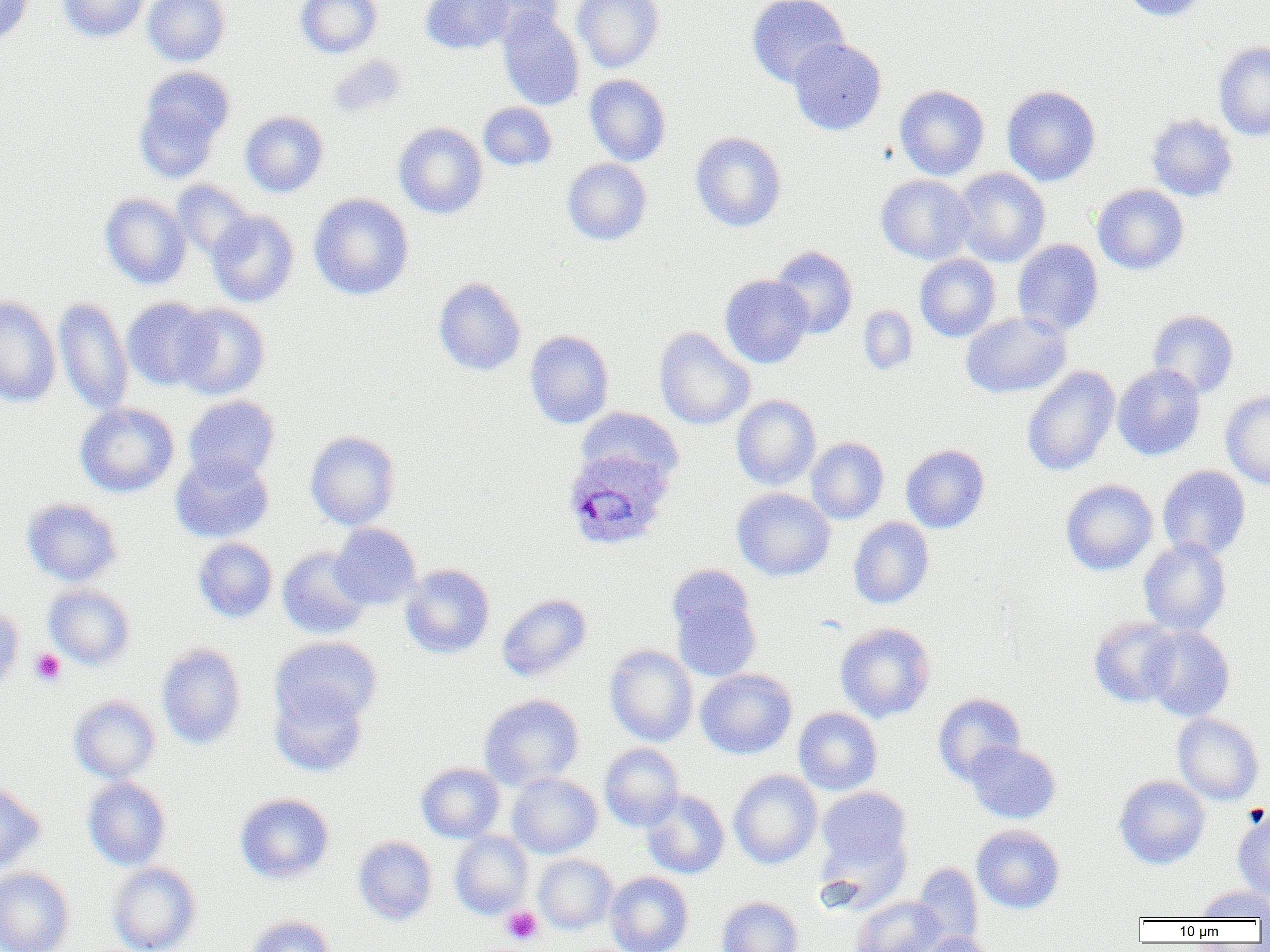

slide-level diagnosis = Plasmodium ovale
platelet locations = approximate bounding boxes as named x1/y1/x2/y2 corners in pixels: (x1=30, y1=648, x2=66, y2=686), (x1=502, y1=906, x2=543, y2=945)
magnification = 1000x
uninfected red blood cell locations = approximate bounding boxes as named x1/y1/x2/y2 corners in pixels: (x1=0, y1=0, x2=34, y2=48), (x1=57, y1=0, x2=151, y2=42), (x1=143, y1=0, x2=230, y2=66), (x1=295, y1=0, x2=382, y2=57), (x1=420, y1=0, x2=513, y2=54), (x1=470, y1=0, x2=563, y2=43), (x1=572, y1=0, x2=664, y2=73), (x1=747, y1=0, x2=849, y2=88), (x1=1118, y1=0, x2=1208, y2=21), (x1=497, y1=9, x2=584, y2=111), (x1=789, y1=38, x2=886, y2=135), (x1=1214, y1=41, x2=1270, y2=140), (x1=327, y1=53, x2=406, y2=118), (x1=134, y1=67, x2=234, y2=179), (x1=584, y1=74, x2=671, y2=166), (x1=894, y1=85, x2=990, y2=180), (x1=1002, y1=85, x2=1101, y2=186), (x1=478, y1=102, x2=556, y2=170), (x1=240, y1=111, x2=328, y2=197), (x1=1146, y1=113, x2=1238, y2=202), (x1=393, y1=122, x2=487, y2=219), (x1=690, y1=131, x2=787, y2=232), (x1=562, y1=158, x2=651, y2=245), (x1=951, y1=168, x2=1050, y2=267), (x1=876, y1=174, x2=975, y2=264), (x1=171, y1=180, x2=254, y2=262), (x1=1092, y1=184, x2=1189, y2=275), (x1=100, y1=193, x2=191, y2=290), (x1=309, y1=193, x2=413, y2=300), (x1=207, y1=211, x2=299, y2=307), (x1=1012, y1=239, x2=1104, y2=336), (x1=770, y1=245, x2=858, y2=339), (x1=914, y1=253, x2=1001, y2=341), (x1=719, y1=274, x2=813, y2=368), (x1=433, y1=277, x2=526, y2=376), (x1=0, y1=295, x2=61, y2=408), (x1=122, y1=297, x2=215, y2=390), (x1=53, y1=298, x2=133, y2=415), (x1=172, y1=304, x2=270, y2=400), (x1=858, y1=306, x2=918, y2=375), (x1=1147, y1=309, x2=1238, y2=398), (x1=960, y1=311, x2=1070, y2=397), (x1=654, y1=327, x2=754, y2=430), (x1=525, y1=330, x2=614, y2=429), (x1=1113, y1=364, x2=1205, y2=461), (x1=1021, y1=366, x2=1120, y2=477), (x1=1220, y1=391, x2=1270, y2=489), (x1=183, y1=395, x2=280, y2=484), (x1=731, y1=395, x2=821, y2=490), (x1=75, y1=403, x2=179, y2=497), (x1=575, y1=407, x2=682, y2=489), (x1=305, y1=431, x2=401, y2=530), (x1=806, y1=437, x2=889, y2=524), (x1=901, y1=444, x2=989, y2=533), (x1=170, y1=453, x2=273, y2=543), (x1=1157, y1=465, x2=1251, y2=560), (x1=1060, y1=479, x2=1158, y2=575), (x1=732, y1=488, x2=835, y2=581), (x1=22, y1=498, x2=122, y2=586), (x1=848, y1=517, x2=934, y2=609), (x1=330, y1=523, x2=421, y2=609), (x1=193, y1=538, x2=277, y2=623), (x1=1138, y1=538, x2=1231, y2=636), (x1=277, y1=546, x2=372, y2=639), (x1=401, y1=564, x2=495, y2=658), (x1=668, y1=571, x2=762, y2=681), (x1=43, y1=584, x2=135, y2=669), (x1=496, y1=593, x2=591, y2=680), (x1=0, y1=605, x2=23, y2=695), (x1=1089, y1=616, x2=1180, y2=707), (x1=835, y1=622, x2=935, y2=722), (x1=1141, y1=626, x2=1235, y2=722), (x1=270, y1=636, x2=382, y2=730), (x1=156, y1=644, x2=247, y2=750), (x1=605, y1=645, x2=698, y2=746), (x1=695, y1=668, x2=797, y2=759), (x1=270, y1=683, x2=368, y2=777), (x1=933, y1=693, x2=1026, y2=783), (x1=479, y1=694, x2=584, y2=790), (x1=68, y1=695, x2=160, y2=784), (x1=793, y1=707, x2=882, y2=795), (x1=1172, y1=714, x2=1263, y2=805), (x1=963, y1=741, x2=1061, y2=824), (x1=599, y1=743, x2=684, y2=831), (x1=416, y1=763, x2=505, y2=842), (x1=729, y1=770, x2=822, y2=869), (x1=507, y1=772, x2=602, y2=859), (x1=1114, y1=775, x2=1210, y2=869), (x1=82, y1=777, x2=171, y2=870), (x1=0, y1=781, x2=45, y2=874), (x1=816, y1=787, x2=910, y2=872), (x1=641, y1=790, x2=729, y2=879), (x1=235, y1=793, x2=334, y2=883), (x1=1233, y1=809, x2=1270, y2=901), (x1=971, y1=824, x2=1065, y2=914), (x1=450, y1=831, x2=533, y2=918), (x1=352, y1=836, x2=437, y2=925), (x1=533, y1=854, x2=617, y2=934), (x1=107, y1=862, x2=201, y2=952), (x1=913, y1=863, x2=984, y2=948), (x1=0, y1=868, x2=74, y2=952), (x1=605, y1=872, x2=693, y2=952), (x1=1196, y1=886, x2=1270, y2=921), (x1=716, y1=896, x2=803, y2=952), (x1=853, y1=896, x2=947, y2=952), (x1=243, y1=915, x2=334, y2=952), (x1=917, y1=931, x2=998, y2=952)
field of view = single
image size = 1270×952 pixels
modality = optical microscopy
Plasmodium ovale-infected red blood cell locations = approximate bounding boxes as named x1/y1/x2/y2 corners in pixels: (x1=563, y1=447, x2=674, y2=551)
preparation = thin blood smear